Give the preparation type.
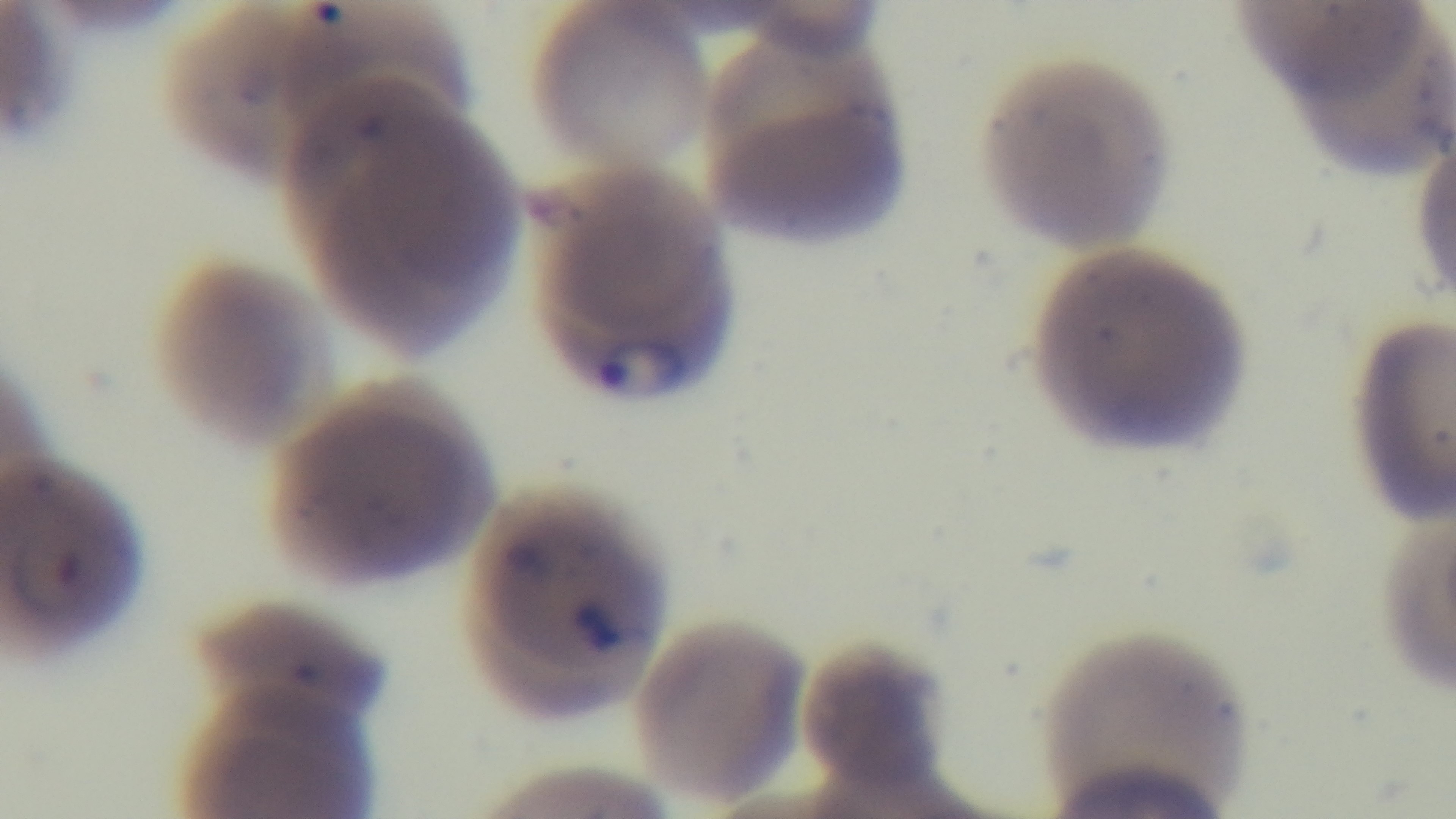

Thin.

Malaria status: infected. Giemsa-stained. Captured with a mounted 4K digital camera. One field from the slide. Light microscopy. Oil-immersion objective, 100x.